Assess this cell for malaria.
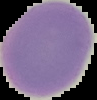

Uninfected.

Summary:
  - Image size: 97×100 pixels
  - Preparation: thin blood film
  - Image type: segmented cell region with the area outside set to black